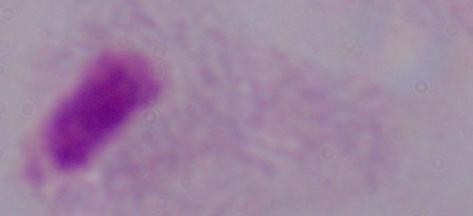

modality = micrograph
identification = trichomonad
magnification = 1000x